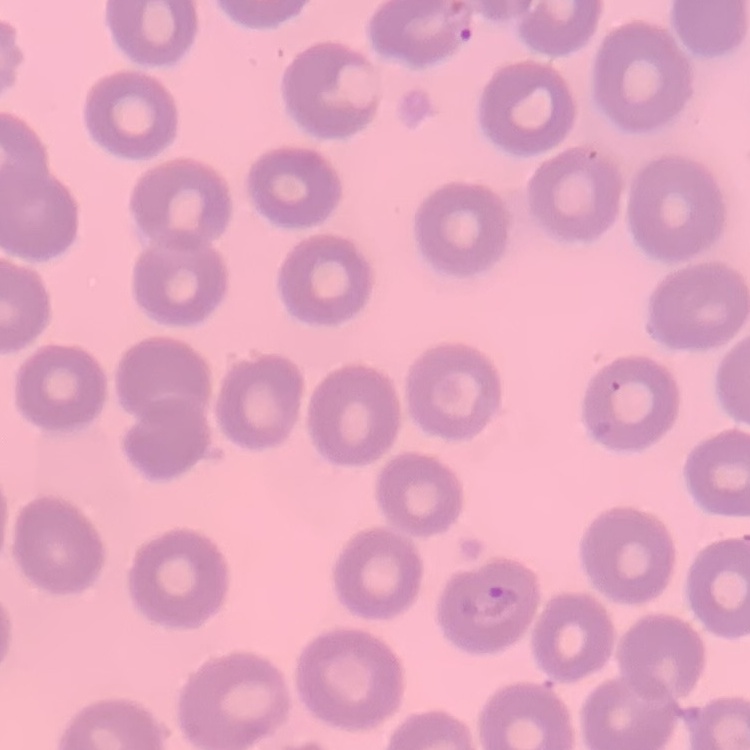
red blood cell morphology = no rouleaux formation
image type = square crop of a larger photomicrograph
stain = Field's or Giemsa
preparation = thin blood film